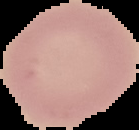

Summary:
  - Preparation: thin blood smear
  - Result: no Plasmodium parasites seen
  - Image size: 139×130 pixels
  - Image type: segmented cell region with the area outside set to black